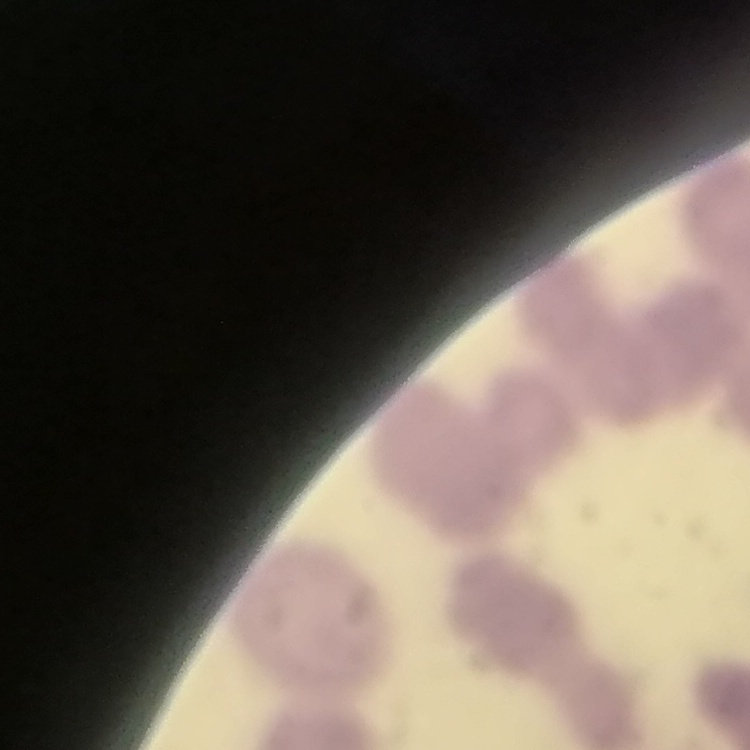

red blood cell morphology = rouleaux formation
stain = Field's or Giemsa
image type = square crop of a larger photomicrograph
preparation = thin peripheral smear